Name the cell type shown.
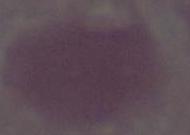

This is an erythrocyte.

{
  "modality": "micrograph",
  "magnification": "1000x"
}